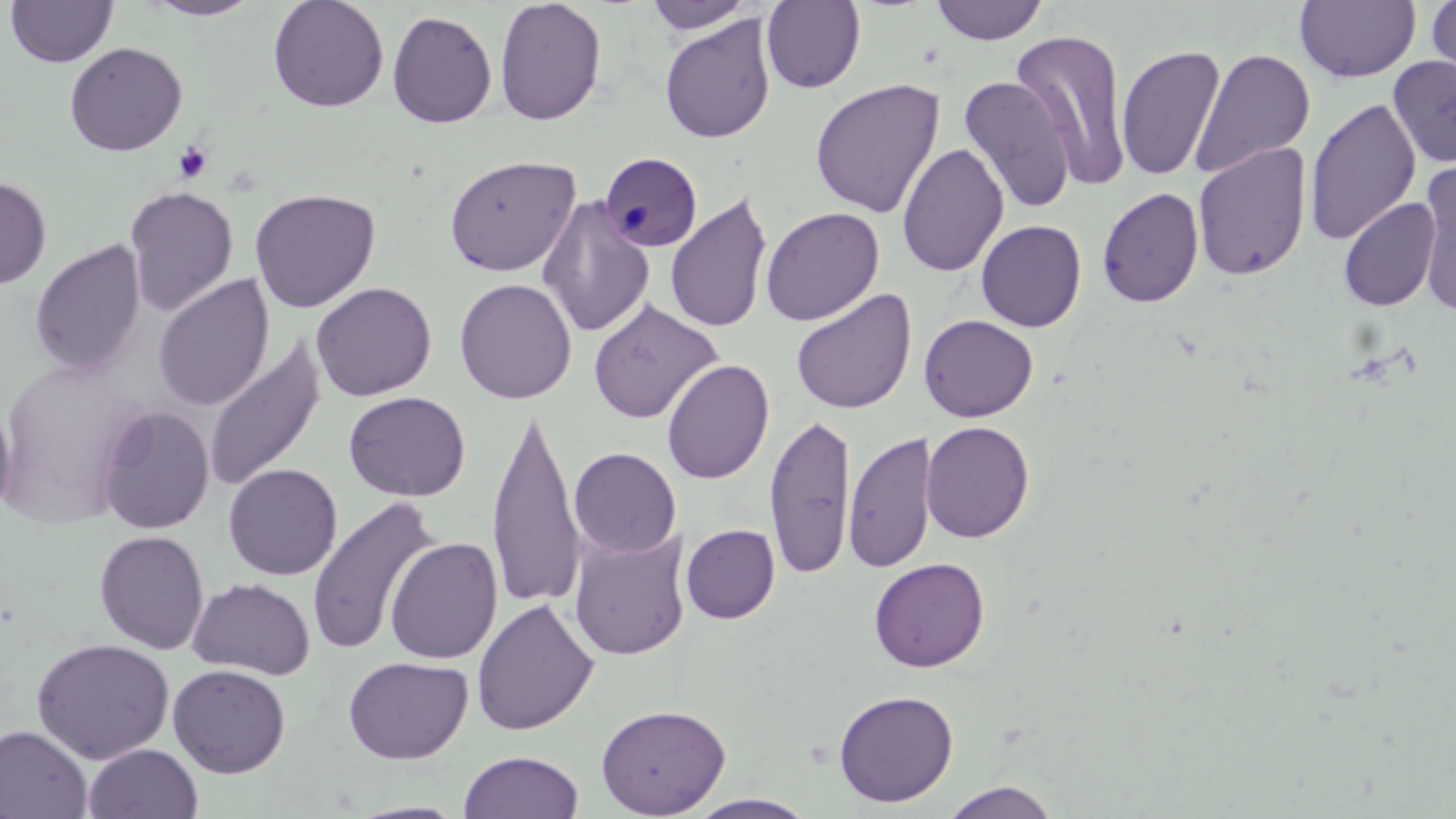

Approximate bounding boxes as [x1, y1, x2, y2] in pixels. Platelet locations: [173, 141, 214, 184]. Plasmodium malariae-infected red blood cell locations: [601, 157, 705, 258]. Uninfected red blood cell locations: [4, 0, 119, 68], [268, 0, 390, 113], [494, 0, 607, 126], [929, 0, 1049, 46], [1427, 0, 1456, 86], [140, 1, 264, 21], [643, 1, 759, 35], [761, 1, 866, 93], [1295, 1, 1421, 84], [387, 9, 498, 129], [659, 15, 776, 144], [1011, 28, 1135, 191], [64, 41, 188, 156], [1116, 43, 1226, 183], [1191, 48, 1315, 180], [1388, 55, 1456, 169], [1357, 66, 1450, 205], [959, 74, 1076, 213], [809, 78, 945, 218], [1304, 97, 1422, 246], [1192, 141, 1311, 281], [897, 142, 1009, 277], [443, 154, 580, 276], [1416, 159, 1456, 319], [0, 174, 52, 290], [124, 185, 239, 317], [249, 187, 381, 313], [1097, 187, 1204, 308], [665, 191, 774, 335], [537, 193, 655, 338], [1338, 197, 1441, 312], [760, 206, 885, 326], [976, 219, 1087, 332], [29, 238, 147, 379], [152, 273, 275, 412], [454, 277, 577, 404], [311, 281, 437, 401], [790, 288, 916, 415], [588, 299, 723, 424], [919, 314, 1038, 422], [203, 336, 326, 494], [0, 357, 148, 525], [661, 358, 775, 485], [344, 390, 471, 501], [0, 393, 16, 523], [97, 405, 215, 534], [487, 407, 586, 611], [764, 411, 856, 580], [921, 420, 1035, 543], [843, 430, 937, 573], [569, 446, 681, 558], [223, 463, 342, 580], [307, 496, 440, 656], [681, 524, 780, 624], [568, 526, 692, 661], [94, 530, 209, 655], [384, 536, 503, 665], [869, 557, 990, 672], [187, 577, 316, 680], [471, 598, 599, 736], [31, 637, 175, 763], [343, 655, 474, 764], [168, 663, 291, 778], [833, 689, 959, 807], [596, 702, 731, 818], [0, 725, 94, 819], [83, 743, 203, 819], [458, 750, 585, 819], [939, 781, 1062, 819], [686, 793, 820, 818], [347, 800, 468, 818]. Slide-level diagnosis: Plasmodium malariae. May-Grünwald-Giemsa-stained preparation. Thin blood smear. Image is 1456×819 pixels. One field of a larger specimen. Light microscopy. 1000x magnification.